Locate every uninfected red blood cell.
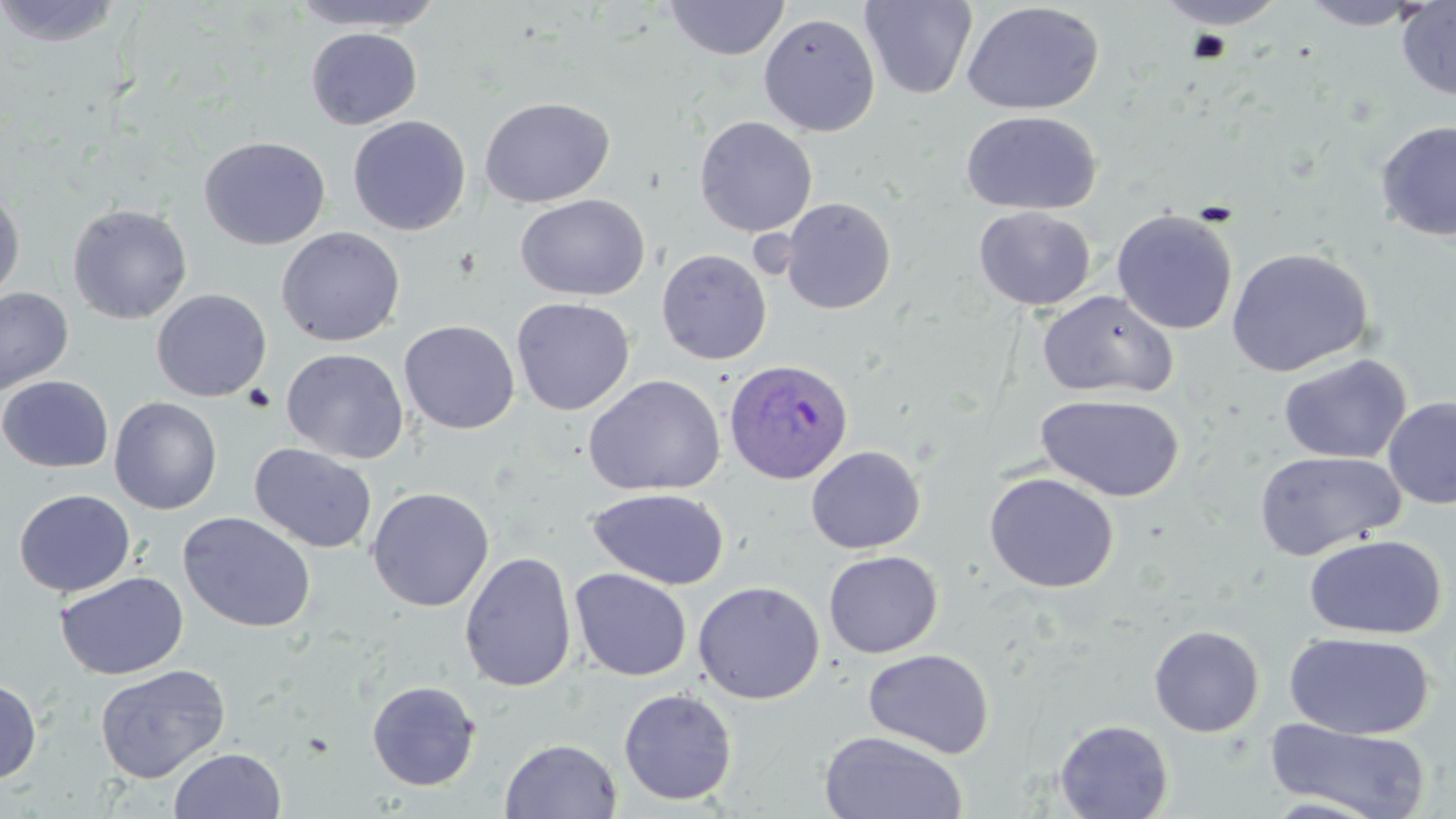
Approximate bounding boxes as (x1, y1, x2, y2) in pixels.
Uninfected red blood cells: (289, 0, 448, 32), (1153, 0, 1291, 29), (1297, 0, 1430, 30), (1396, 0, 1456, 101), (0, 1, 127, 48), (663, 1, 790, 60), (860, 1, 978, 100), (962, 1, 1104, 116), (758, 12, 880, 137), (305, 27, 424, 129), (479, 96, 614, 208), (961, 110, 1102, 215), (347, 115, 471, 236), (694, 116, 818, 237), (1374, 120, 1456, 242), (199, 136, 330, 250), (0, 186, 25, 304), (515, 194, 651, 301), (780, 197, 896, 314), (67, 203, 192, 324), (974, 206, 1096, 311), (1111, 209, 1238, 335), (276, 226, 405, 347), (1225, 247, 1375, 377), (656, 248, 772, 365), (0, 287, 74, 397), (151, 289, 272, 402), (1036, 290, 1178, 399), (511, 297, 635, 415), (399, 319, 520, 434), (281, 347, 409, 464), (1278, 353, 1412, 464), (583, 374, 726, 497), (0, 375, 114, 473), (1035, 394, 1185, 502), (109, 396, 223, 514), (1382, 398, 1456, 510), (249, 443, 377, 554), (806, 445, 926, 554), (1254, 449, 1408, 561), (983, 472, 1119, 593), (367, 487, 494, 612), (587, 487, 730, 590), (13, 488, 136, 597), (178, 511, 317, 633), (1304, 534, 1446, 639), (459, 551, 577, 693), (823, 551, 943, 658), (570, 568, 692, 681), (55, 571, 189, 680), (692, 580, 825, 704), (1148, 625, 1265, 737), (1284, 632, 1435, 741), (863, 648, 994, 759), (94, 663, 231, 783), (0, 678, 42, 785), (366, 680, 481, 791), (618, 687, 738, 806), (1054, 718, 1173, 819), (1265, 718, 1432, 819), (817, 730, 969, 819), (500, 738, 622, 818), (168, 747, 287, 818).

{
  "slide_level_diagnosis": "Plasmodium ovale",
  "modality": "light microscopy",
  "field_of_view": "one of a larger specimen",
  "plasmodium_ovale_infected_red_blood_cell_locations": "approximate bounding boxes as (x1, y1, x2, y2) in pixels: (723, 359, 854, 485)",
  "preparation": "thin blood film",
  "image_size": "1456×819 pixels",
  "stain": "May-Grünwald-Giemsa",
  "magnification": "1000x"
}